Locate and identify every blood parasite.
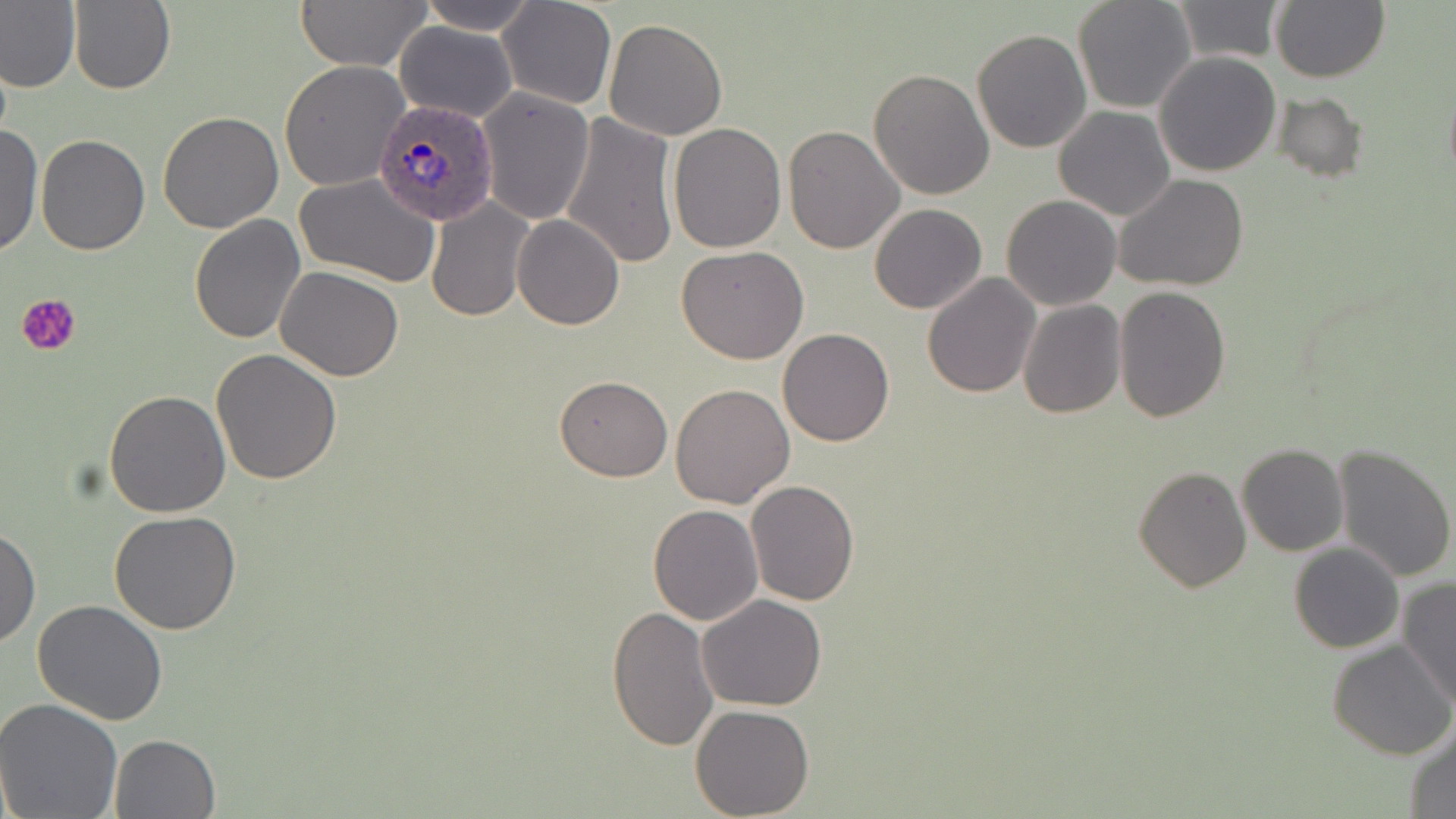
Approximate bounding boxes as (x1, y1, x2, y2) in pixels.
Plasmodium ovale-infected red blood cells: (372, 100, 500, 228).
No Plasmodium falciparum, Plasmodium malariae, Plasmodium vivax, Babesia divergens, or Trypanosoma brucei observed.

{
  "slide_level_diagnosis": "Plasmodium ovale",
  "image_size": "1456×819 pixels",
  "preparation": "thin blood film",
  "uninfected_red_blood_cell_locations": "approximate bounding boxes as (x1, y1, x2, y2) in pixels: (0, 0, 82, 94), (68, 0, 175, 96), (293, 0, 432, 71), (413, 0, 541, 34), (1072, 0, 1196, 115), (1271, 0, 1390, 83), (496, 1, 616, 110), (1171, 1, 1284, 63), (602, 17, 728, 140), (394, 20, 518, 122), (970, 28, 1091, 154), (1153, 51, 1282, 176), (278, 60, 410, 192), (868, 69, 995, 200), (477, 88, 595, 225), (1273, 90, 1367, 182), (786, 100, 986, 234), (1053, 106, 1177, 220), (157, 111, 284, 233), (559, 113, 678, 270), (667, 122, 786, 252), (0, 123, 43, 260), (784, 124, 906, 253), (36, 133, 151, 255), (294, 172, 442, 287), (1114, 173, 1248, 292), (1001, 195, 1122, 312), (426, 198, 533, 321), (869, 204, 988, 314), (189, 214, 306, 342), (512, 214, 625, 329), (677, 244, 809, 365), (276, 266, 405, 382), (922, 271, 1040, 398), (1113, 285, 1231, 423), (1017, 300, 1126, 417), (776, 328, 894, 447), (212, 348, 343, 484), (554, 375, 673, 482), (670, 384, 795, 508), (104, 389, 232, 518), (1236, 444, 1348, 557), (1333, 444, 1455, 582), (1134, 465, 1250, 591), (747, 480, 860, 607), (647, 504, 763, 625), (109, 510, 242, 633), (0, 525, 40, 650), (1289, 542, 1404, 654), (1398, 578, 1455, 709), (697, 594, 827, 711), (32, 598, 168, 725), (606, 604, 719, 751), (1327, 638, 1456, 760), (0, 699, 126, 819), (689, 703, 815, 818), (1405, 722, 1456, 818), (108, 732, 219, 818)",
  "field_of_view": "single",
  "platelet_locations": "approximate bounding boxes as (x1, y1, x2, y2) in pixels: (18, 293, 81, 356)",
  "magnification": "1000x",
  "modality": "light microscopy",
  "stain": "May-Grünwald-Giemsa"
}